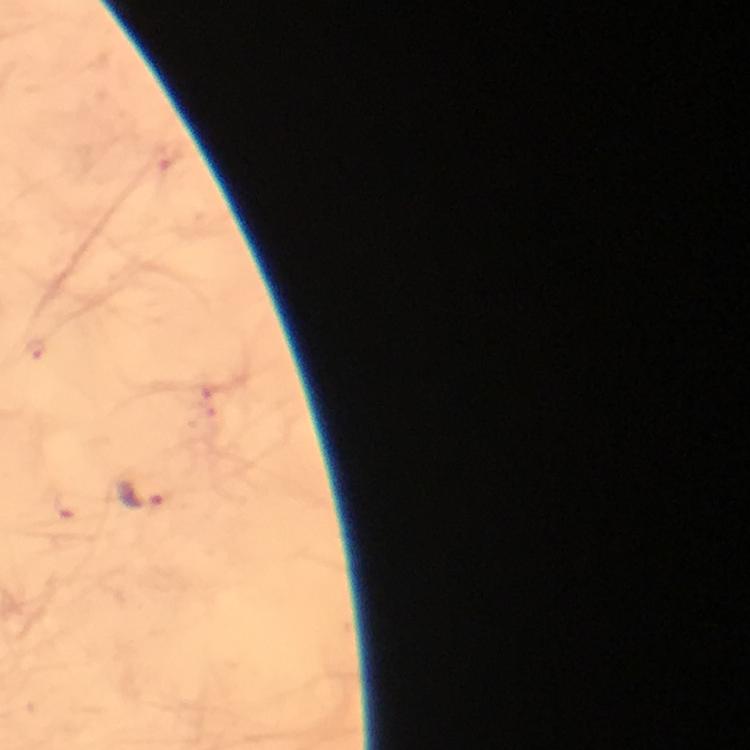
preparation = thick smear
immersion oil = applied
magnification = 100x
stain = Giemsa
Plasmodium parasite locations = approximate centers as {x, y} in pixels: {36, 347}, {138, 493}
capture = smartphone camera through the microscope
image size = 750×750 pixels
context = from a malaria diagnostic workup
cropped from = one field of view